Name the parasite shown.
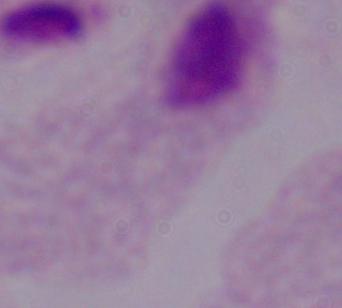
A trichomonad.

magnification: 1000x
modality: micrograph